Outline each blood parasite and name the species.
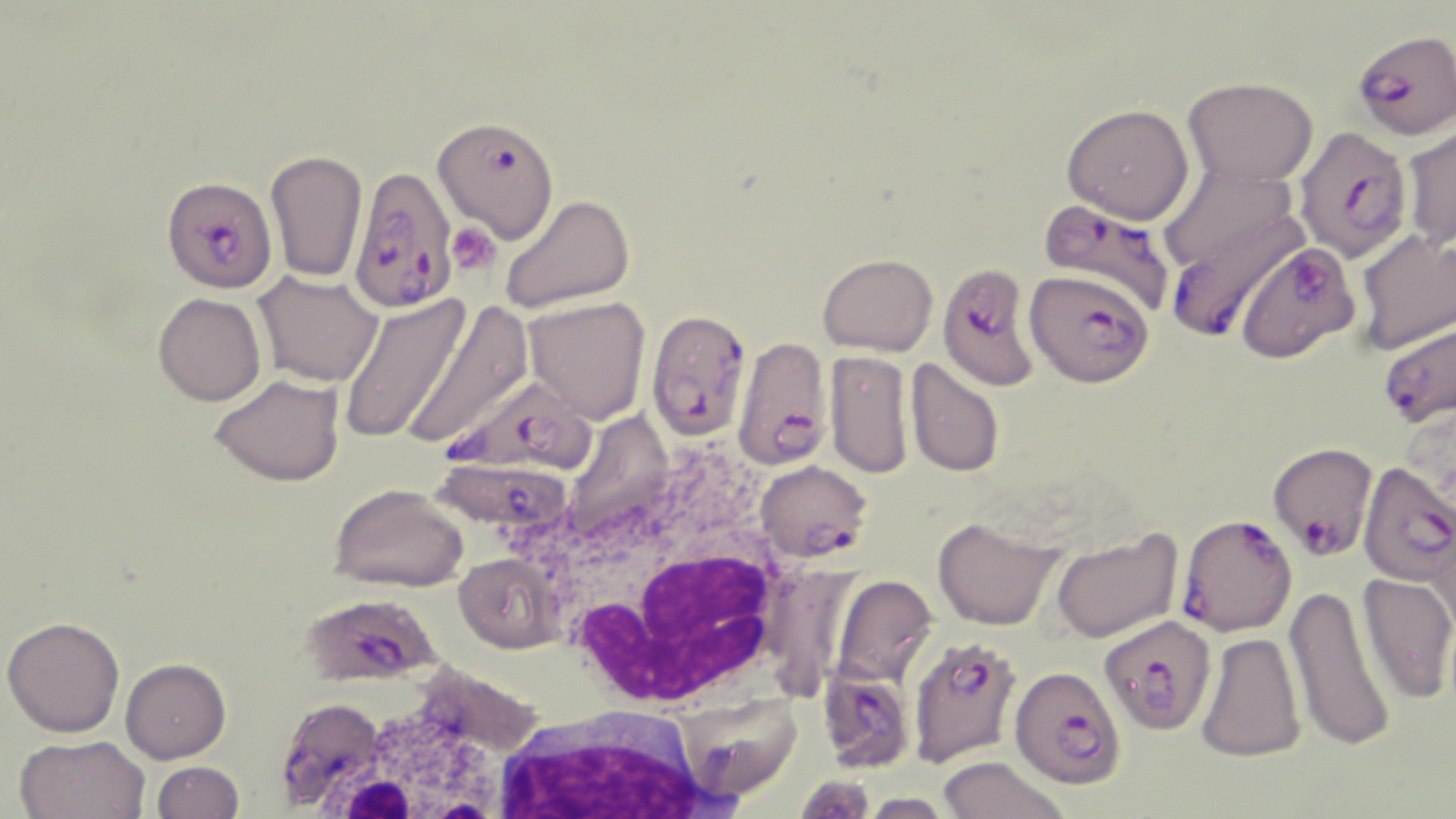

Approximate bounding boxes as (x1,y1)-(x2,y2) corner pairs in pixels.
Plasmodium falciparum-infected red blood cells: (1353,28)-(1456,139), (438,123)-(562,255), (1293,126)-(1414,263), (348,165)-(458,313), (161,176)-(277,293), (1039,198)-(1175,317), (1163,199)-(1308,342), (1234,241)-(1360,363), (937,262)-(1038,390), (1025,268)-(1154,387), (646,308)-(751,442), (1378,320)-(1456,429), (731,336)-(834,472), (441,373)-(600,477), (1268,442)-(1377,559), (431,454)-(578,545), (755,460)-(872,562), (1358,461)-(1456,588), (1176,513)-(1297,638), (300,593)-(442,687), (1100,615)-(1217,735), (908,636)-(1024,767), (818,665)-(916,773), (1009,665)-(1126,789), (273,697)-(394,812).
No Plasmodium ovale, Plasmodium malariae, Plasmodium vivax, Babesia divergens, or Trypanosoma brucei observed.

Summary:
  - White blood cell locations: (541,477)-(794,708), (293,676)-(542,817), (490,704)-(722,819)
  - Uninfected red blood cell locations: (1183,76)-(1318,187), (1061,103)-(1194,224), (1401,121)-(1456,249), (265,148)-(369,283), (1156,162)-(1303,281), (501,193)-(635,313), (1354,229)-(1456,355), (817,253)-(938,355), (253,271)-(382,388), (153,292)-(266,406), (335,293)-(471,445), (522,296)-(650,424), (402,300)-(535,451), (825,350)-(913,479), (904,358)-(1005,478), (210,374)-(346,486), (329,483)-(468,592), (1427,515)-(1456,644), (932,516)-(1063,630), (1049,529)-(1184,644), (454,553)-(564,653), (1357,572)-(1456,706), (831,576)-(938,686), (1284,584)-(1397,754), (2,616)-(125,737), (1195,631)-(1306,762), (120,656)-(231,763), (673,692)-(802,801), (14,734)-(150,819), (937,755)-(1072,818), (151,760)-(245,818), (793,774)-(877,818), (856,792)-(959,818)
  - Platelet locations: (446,221)-(502,276)
  - Slide-level diagnosis: Plasmodium falciparum
  - Preparation: thin blood smear
  - Stain: May-Grünwald-Giemsa
  - Field of view: single
  - Image size: 1456×819 pixels
  - Modality: light microscopy
  - Magnification: 1000x